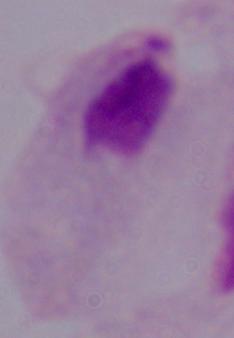

Captured at 1000x magnification. Photomicrograph. A trichomonad is seen.